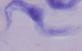
Summary:
  - Modality: photomicrograph
  - Magnification: 1000x
  - Identification: trypanosome